Comment on the morphology of the erythrocytes.
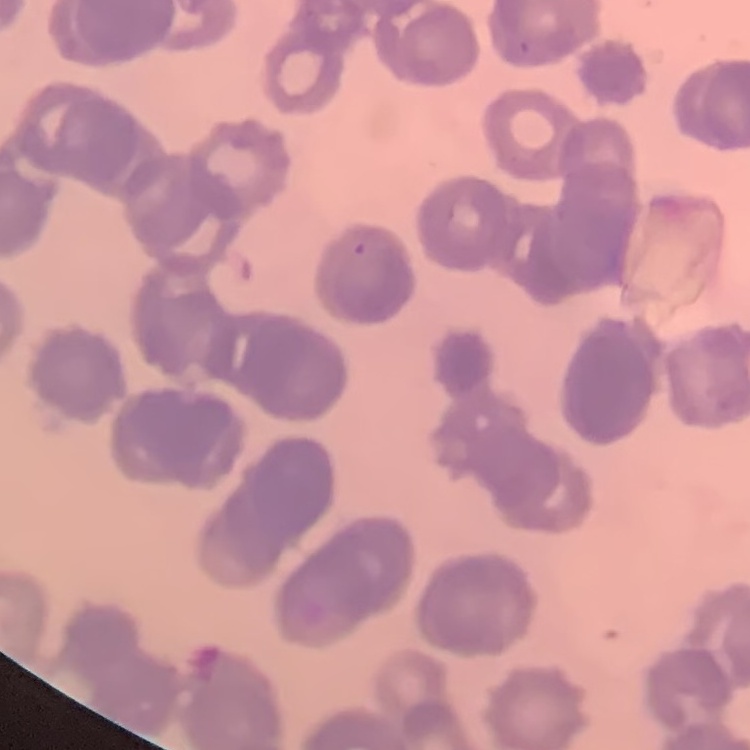
Rouleaux formation.

preparation: thin blood smear
stain: Field's or Giemsa
image_type: square crop of a larger photomicrograph